Classify this cell by malaria status.
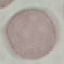
It is uninfected.

{
  "capture": "smartphone camera at the microscope eyepiece",
  "preparation": "thin blood film",
  "stain": "Giemsa",
  "image_type": "cell patch, automatically extracted from a larger field of view and resized to 64 × 64 pixels"
}